Give the position of every leukocyte visible.
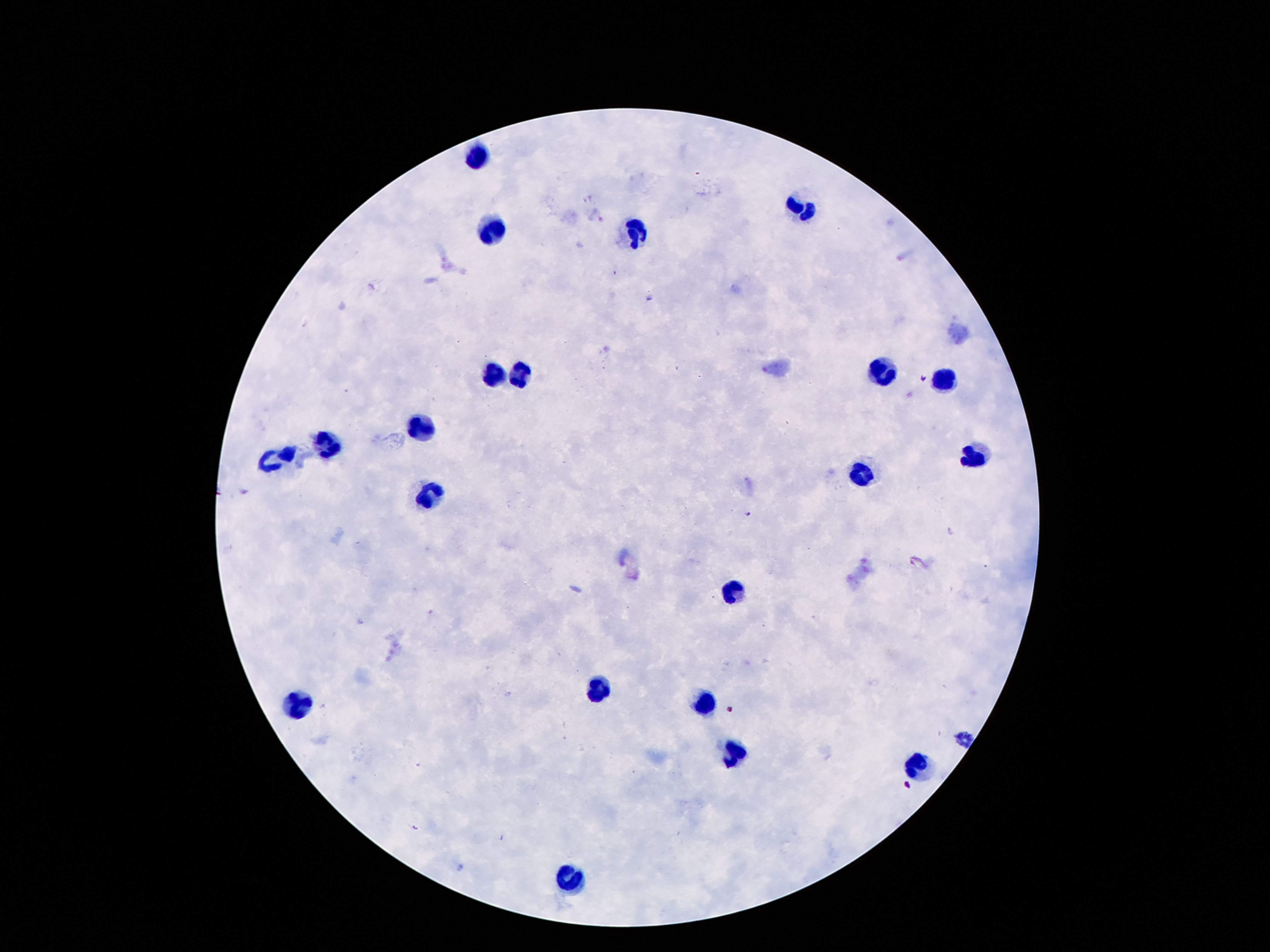
Approximate centers as {x, y} in pixels.
Leukocytes: {480, 158}, {803, 208}, {491, 235}, {635, 235}, {493, 371}, {881, 371}, {519, 373}, {943, 381}, {424, 429}, {327, 447}, {275, 455}, {971, 455}, {864, 475}, {428, 492}, {739, 592}, {596, 691}, {292, 702}, {702, 708}, {732, 755}, {915, 770}, {568, 876}.

Image is 1270×952 pixels. Patient malaria status: negative. Thick blood film. 100x magnification. Smartphone photograph taken through the microscope eyepiece. One field from this slide. Giemsa-stained preparation.